Outline each blood parasite and name the species.
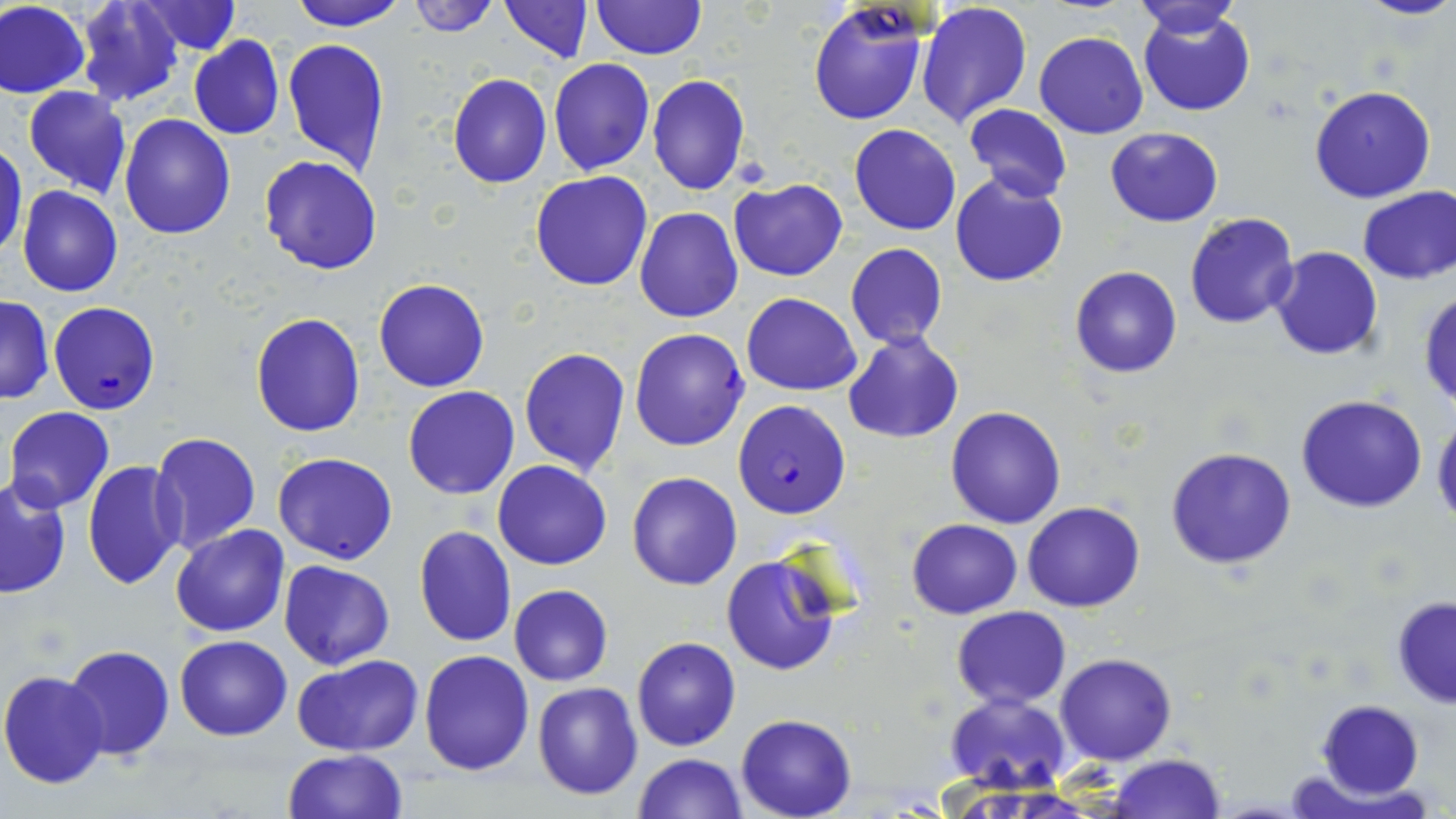

Approximate bounding boxes as (x1,y1)-(x2,y2) corner pairs in pixels.
Plasmodium falciparum-infected red blood cells: (48,301)-(163,415), (628,326)-(749,451), (733,399)-(851,519).
No Plasmodium ovale, Plasmodium malariae, Plasmodium vivax, Babesia divergens, or Trypanosoma brucei observed.

Summary:
  - Uninfected red blood cell locations: (289,0)-(406,30), (406,0)-(500,37), (498,0)-(591,62), (590,0)-(707,61), (1133,0)-(1242,38), (1351,0)-(1456,22), (0,1)-(89,99), (75,1)-(184,107), (134,1)-(240,55), (918,3)-(1033,130), (808,4)-(927,127), (1,6)-(167,121), (1137,8)-(1255,117), (1034,30)-(1149,138), (188,35)-(285,139), (282,35)-(390,175), (548,59)-(654,175), (447,74)-(552,189), (647,74)-(749,194), (1309,85)-(1436,203), (23,87)-(131,198), (964,104)-(1072,202), (119,114)-(236,239), (850,124)-(961,236), (1105,126)-(1222,227), (0,144)-(27,261), (259,155)-(383,274), (531,171)-(653,292), (951,174)-(1068,289), (728,179)-(848,280), (1356,185)-(1456,284), (17,187)-(123,297), (634,208)-(743,324), (1185,212)-(1300,328), (845,244)-(949,350), (1270,246)-(1384,360), (1070,265)-(1181,379), (374,278)-(490,392), (1418,289)-(1456,410), (741,292)-(863,394), (0,296)-(53,404), (251,312)-(365,437), (842,332)-(965,444), (518,347)-(632,476), (403,386)-(519,499), (1297,394)-(1428,513), (4,406)-(115,513), (945,406)-(1067,529), (1431,414)-(1456,529), (150,432)-(261,554), (1164,447)-(1298,569), (272,452)-(398,565), (82,459)-(186,589), (492,460)-(612,569), (626,471)-(744,591), (1,479)-(72,597), (1023,501)-(1145,612), (906,518)-(1023,619), (171,525)-(289,637), (413,525)-(516,647), (722,554)-(843,675), (279,561)-(395,669), (509,585)-(613,686), (1389,596)-(1456,708), (952,606)-(1072,709), (176,634)-(292,740), (631,636)-(740,751), (63,645)-(176,762), (420,649)-(535,776), (1055,652)-(1177,766), (292,655)-(425,757), (0,671)-(112,789), (532,681)-(643,800), (944,692)-(1072,793), (1317,700)-(1423,799), (735,714)-(856,819), (283,749)-(407,819), (1108,753)-(1225,818), (632,754)-(747,819)
  - Slide-level diagnosis: Plasmodium falciparum
  - Field of view: single
  - Image size: 1456×819 pixels
  - Magnification: 1000x
  - Modality: optical microscopy
  - Preparation: thin blood film
  - Stain: May-Grünwald-Giemsa